Point out each Plasmodium parasite.
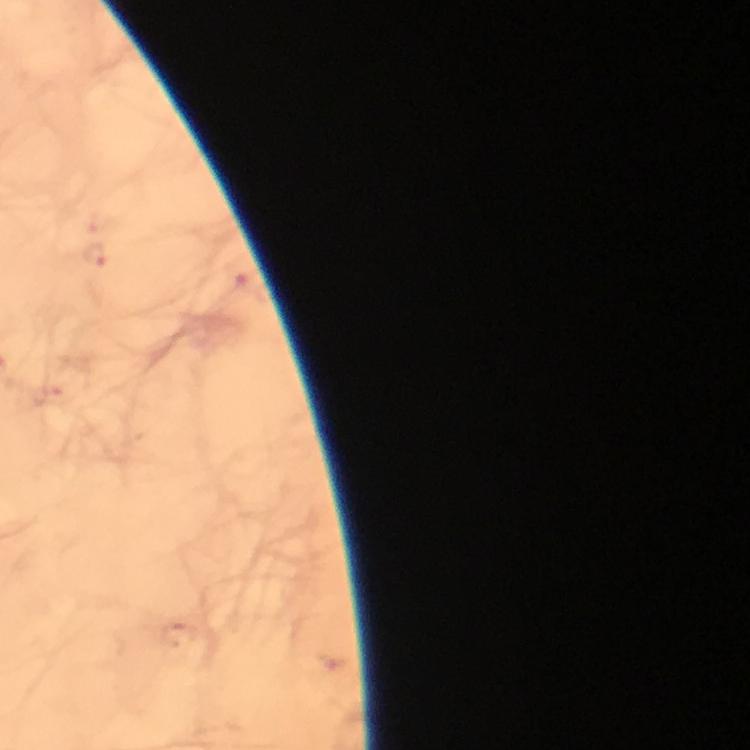

Approximate centers as {x, y} in pixels.
Plasmodium parasites: {95, 255}.

Thick blood smear. From a malaria diagnostic workup. 100x magnification. Immersion oil was used. Photographed with a smartphone mounted on the microscope. A crop from one field of view. Giemsa-stained preparation. Image is 750×750 pixels.